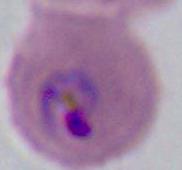
Summary:
  - Magnification: 400x or 1000x
  - Identification: Plasmodium
  - Modality: micrograph